Find each parasitized RBC.
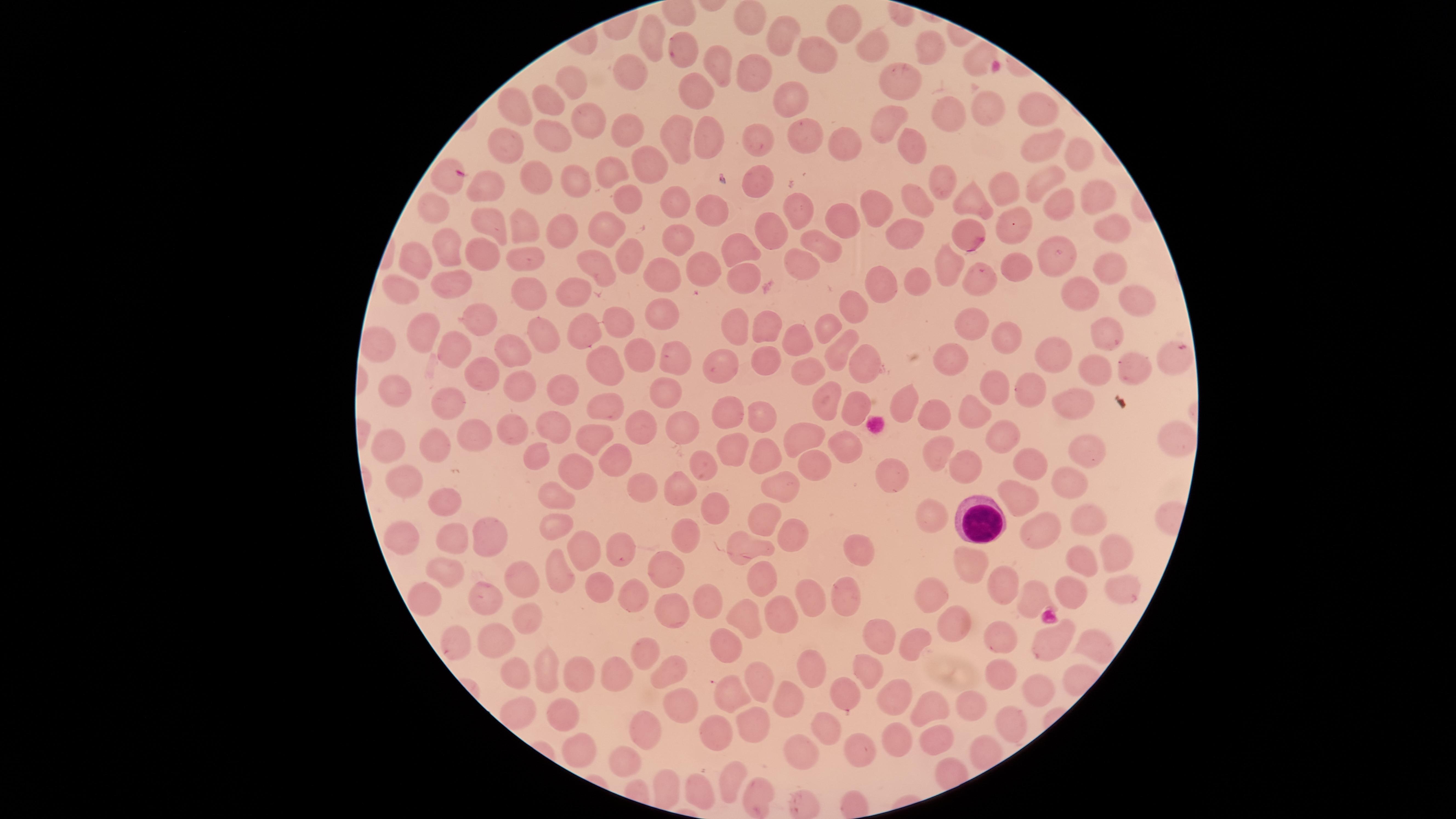
No parasitized RBCs identified.

preparation = thin blood smear
WBCs = approximate marker points as {x, y} in pixels: {983, 522}
image size = 1456×819 pixels
visible region = circular
stain = Giemsa
uninfected RBCs = approximate marker points as {x, y} in pixels: {751, 21}, {847, 21}, {791, 31}, {654, 35}, {875, 43}, {823, 44}, {927, 46}, {685, 51}, {980, 59}, {713, 63}, {629, 72}, {750, 73}, {904, 80}, {701, 89}, {572, 90}, {552, 98}, {789, 99}, {1042, 104}, {526, 106}, {979, 114}, {883, 116}, {944, 116}, {590, 119}, {624, 127}, {556, 129}, {707, 133}, {678, 134}, {1042, 135}, {511, 136}, {754, 136}, {801, 140}, {840, 144}, {915, 148}, {1081, 157}, {647, 162}, {609, 165}, {534, 175}, {451, 180}, {573, 180}, {952, 181}, {1045, 181}, {763, 182}, {1013, 185}, {496, 194}, {978, 194}, {632, 196}, {432, 202}, {1062, 202}, {1097, 202}, {681, 204}, {918, 204}, {707, 208}, {806, 208}, {879, 208}, {840, 216}, {1019, 217}, {485, 219}, {529, 227}, {1107, 227}, {566, 229}, {771, 229}, {607, 232}, {963, 234}, {899, 237}, {675, 241}, {745, 245}, {826, 246}, {473, 247}, {451, 248}, {1067, 250}, {632, 254}, {423, 256}, {519, 257}, {797, 263}, {946, 263}, {1112, 263}, {1024, 265}, {605, 266}, {705, 266}, {670, 271}, {744, 273}, {886, 275}, {922, 277}, {987, 281}, {408, 285}, {451, 285}, {581, 285}, {1089, 286}, {531, 293}, {1133, 299}, {850, 305}, {657, 314}, {481, 320}, {613, 321}, {737, 322}, {979, 323}, {580, 325}, {771, 325}, {833, 325}, {1106, 325}, {543, 327}, {435, 328}, {1013, 333}, {797, 340}, {455, 345}, {1057, 349}, {840, 351}, {512, 352}, {641, 352}, {951, 353}, {771, 355}, {1172, 355}, {723, 357}, {676, 363}, {863, 363}, {604, 364}, {1099, 364}, {1137, 367}, {810, 370}, {483, 377}, {516, 384}, {561, 386}, {402, 387}, {1003, 387}, {1036, 390}, {665, 394}, {825, 400}, {449, 403}, {1081, 403}, {911, 404}, {596, 407}, {857, 407}, {973, 412}, {759, 418}, {937, 418}, {726, 420}, {633, 424}, {554, 427}, {682, 427}, {510, 430}, {473, 432}, {1177, 432}, {595, 436}, {807, 438}, {993, 441}, {432, 443}, {845, 444}, {385, 445}, {1084, 446}, {732, 449}, {537, 451}, {940, 452}, {756, 457}, {1029, 463}, {610, 464}, {704, 464}, {574, 466}, {819, 467}, {898, 467}, {962, 471}, {398, 480}, {787, 481}, {1069, 482}, {674, 489}, {556, 490}, {641, 490}, {1021, 495}, {440, 501}, {714, 510}, {770, 514}, {940, 516}, {1085, 516}, {490, 528}, {550, 528}, {1053, 531}, {685, 534}, {791, 534}, {450, 537}, {398, 538}, {750, 543}, {582, 547}, {612, 547}, {860, 549}, {1115, 552}, {1086, 557}, {982, 561}, {558, 564}, {667, 567}, {443, 572}, {525, 575}, {762, 581}, {1080, 583}, {1119, 585}, {597, 586}, {1012, 588}, {420, 591}, {930, 592}, {816, 593}, {849, 596}, {487, 597}, {634, 597}, {1039, 597}, {712, 598}, {664, 606}, {746, 611}, {779, 612}, {536, 619}, {947, 620}, {885, 638}, {917, 639}, {995, 639}, {450, 641}, {485, 645}, {729, 646}, {1043, 651}, {1093, 651}, {644, 655}, {577, 668}, {1003, 668}, {544, 670}, {813, 670}, {670, 671}, {618, 673}, {514, 674}, {875, 678}, {764, 679}, {1043, 686}, {733, 690}, {896, 698}, {679, 701}, {854, 703}, {793, 704}, {975, 705}, {517, 712}, {935, 713}, {552, 717}, {1012, 720}, {755, 722}, {641, 730}, {825, 730}, {720, 731}, {944, 737}, {901, 742}, {856, 746}, {575, 749}, {803, 754}, {631, 761}, {731, 779}, {698, 790}, {760, 790}
field of view = single
capture = smartphone photograph through the microscope eyepiece